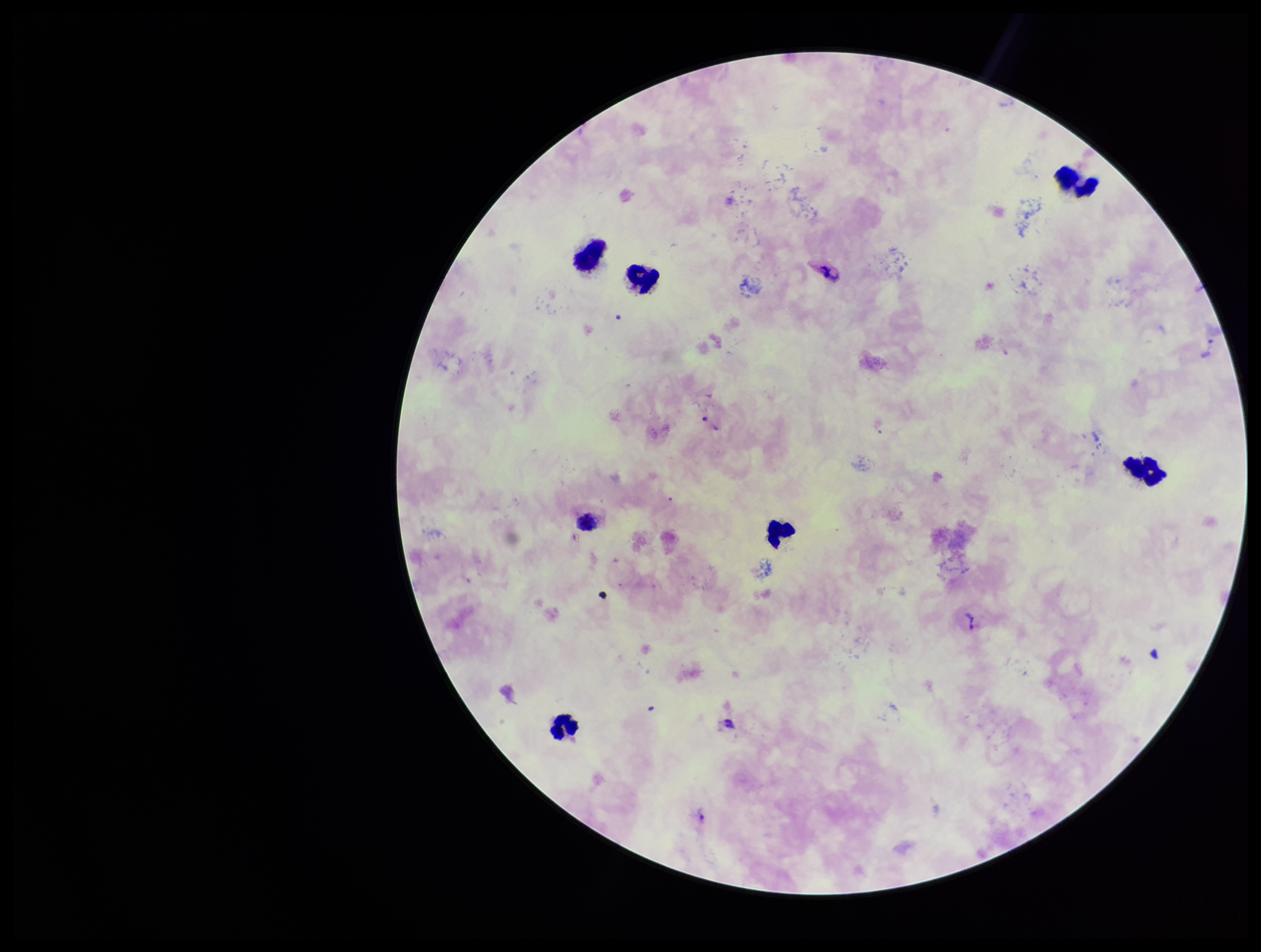

Summary:
  - Parasite count: 2
  - Image size: 1261×952 pixels
  - Plasmodium parasites: identified
  - Species reported for this patient: Plasmodium vivax
  - Field of view: single
  - Patient malaria status: infected
  - Leukocyte count: 7
  - Stain: Giemsa
  - Capture: smartphone photograph through the microscope eyepiece
  - Preparation: thick blood smear